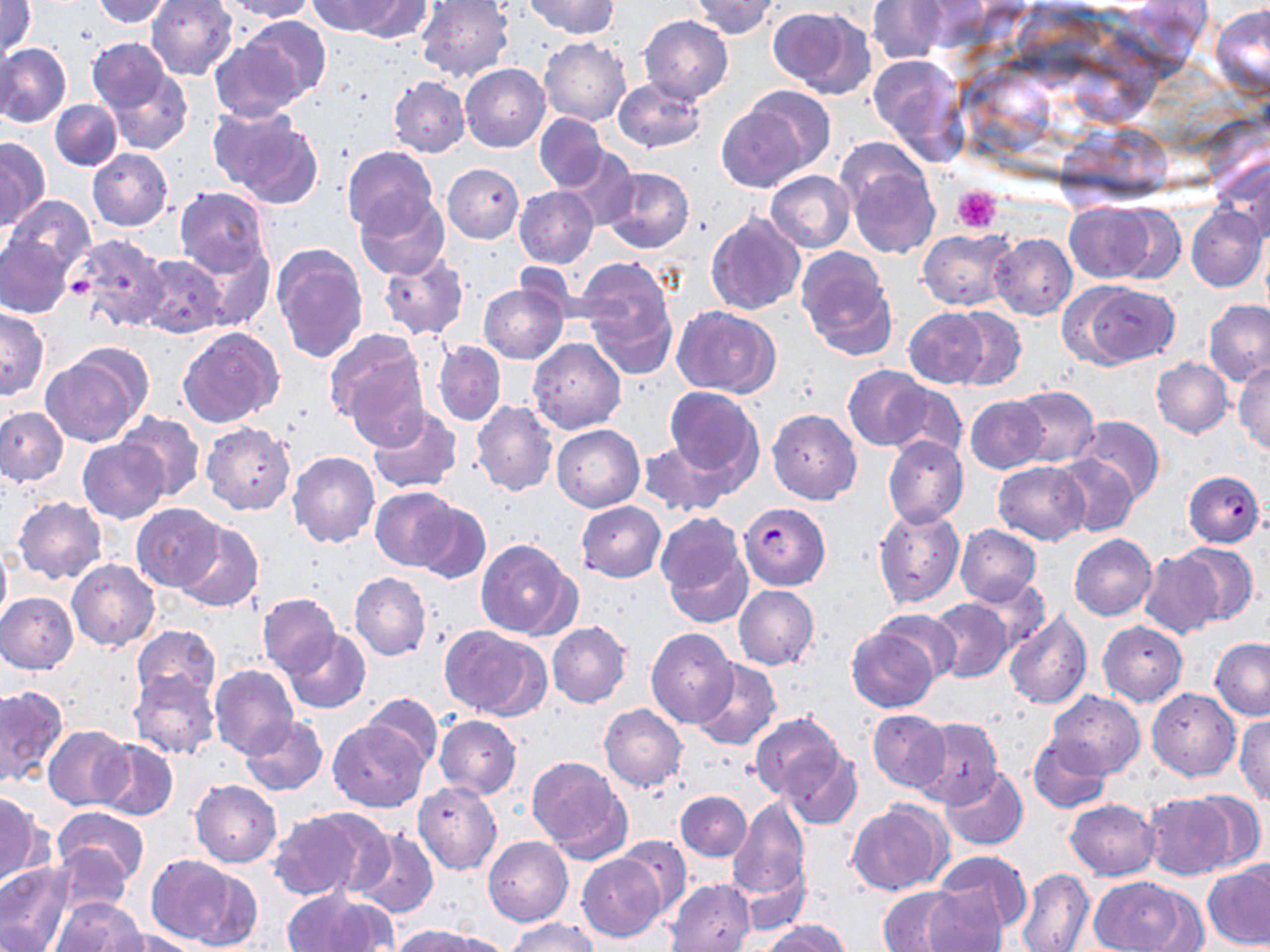

Summary:
  - Coordinate format: approximate bounding boxes as [x1, y1, x2, y2] in pixels
  - Plasmodium falciparum-infected red blood cell locations: [1183, 470, 1265, 546], [738, 501, 831, 590]
  - Platelet locations: [951, 186, 1003, 236], [68, 277, 97, 300]
  - Uninfected red blood cell locations: [92, 0, 172, 26], [146, 0, 239, 81], [219, 0, 315, 21], [306, 0, 406, 36], [343, 0, 432, 40], [523, 0, 619, 39], [689, 0, 780, 39], [867, 0, 946, 64], [1, 1, 37, 62], [415, 1, 514, 81], [1212, 4, 1269, 97], [768, 5, 876, 99], [238, 15, 333, 108], [639, 15, 733, 104], [539, 37, 631, 126], [87, 38, 169, 111], [209, 39, 306, 122], [0, 40, 18, 121], [1, 43, 72, 128], [867, 53, 970, 162], [461, 63, 551, 153], [107, 67, 192, 155], [98, 68, 182, 230], [388, 77, 469, 158], [614, 78, 706, 152], [715, 98, 812, 192], [50, 100, 122, 170], [209, 106, 322, 207], [535, 114, 608, 191], [0, 136, 49, 228], [560, 144, 638, 231], [341, 146, 437, 235], [87, 148, 173, 231], [1213, 153, 1270, 243], [843, 156, 939, 258], [443, 163, 524, 243], [602, 166, 693, 254], [766, 170, 855, 253], [174, 186, 271, 278], [515, 186, 599, 268], [355, 190, 450, 279], [4, 197, 93, 278], [1065, 204, 1156, 283], [1105, 205, 1185, 284], [1186, 206, 1268, 292], [706, 212, 804, 315], [918, 229, 1016, 310], [69, 233, 169, 331], [990, 234, 1077, 321], [1, 237, 74, 317], [272, 244, 369, 363], [188, 245, 274, 330], [795, 249, 896, 359], [376, 250, 468, 341], [136, 254, 226, 338], [574, 257, 678, 372], [1069, 281, 1177, 369], [478, 283, 570, 363], [1203, 300, 1270, 386], [672, 306, 780, 396], [903, 307, 989, 388], [949, 307, 1026, 391], [0, 309, 49, 400], [178, 326, 284, 427], [325, 329, 428, 436], [529, 339, 625, 434], [433, 341, 506, 427], [41, 347, 151, 446], [1152, 357, 1233, 437], [1234, 361, 1269, 455], [843, 366, 930, 451], [883, 383, 967, 464], [1010, 385, 1099, 467], [665, 386, 760, 483], [965, 396, 1048, 473], [472, 402, 558, 497], [367, 406, 462, 494], [0, 407, 68, 487], [768, 409, 862, 505], [116, 412, 205, 501], [1073, 415, 1163, 504], [202, 422, 295, 515], [552, 424, 644, 511], [882, 436, 969, 528], [77, 437, 169, 524], [638, 438, 734, 516], [288, 452, 380, 548], [1052, 452, 1137, 537], [994, 461, 1091, 545], [370, 487, 460, 572], [13, 497, 107, 584], [413, 499, 490, 584], [576, 501, 666, 581], [132, 503, 225, 591], [873, 506, 964, 609], [656, 511, 751, 624], [173, 520, 264, 613], [955, 524, 1041, 605], [1069, 533, 1157, 620], [475, 539, 579, 640], [0, 542, 11, 631], [1171, 542, 1258, 626], [1139, 551, 1222, 638], [66, 558, 160, 650], [350, 572, 431, 660], [965, 577, 1046, 655], [733, 585, 819, 670], [0, 592, 78, 674], [257, 593, 341, 676], [928, 598, 1011, 682], [872, 606, 963, 683], [1004, 610, 1092, 710], [1098, 620, 1188, 706], [547, 621, 631, 707], [130, 625, 220, 706], [846, 625, 940, 713], [443, 626, 551, 720], [646, 628, 737, 728], [283, 629, 370, 714], [1209, 638, 1270, 719], [691, 659, 780, 750], [209, 664, 298, 757], [129, 672, 219, 759], [0, 686, 66, 787], [1147, 688, 1240, 780], [1047, 690, 1143, 778], [360, 693, 442, 772], [600, 704, 687, 792], [868, 709, 951, 793], [749, 712, 848, 807], [435, 715, 521, 799], [1234, 715, 1270, 805], [240, 717, 328, 797], [911, 718, 1002, 807], [329, 720, 425, 812], [42, 725, 132, 810], [1027, 732, 1113, 814], [94, 740, 177, 821], [780, 747, 862, 829], [527, 755, 631, 860], [940, 766, 1028, 851], [189, 780, 282, 867], [413, 781, 502, 875], [676, 789, 752, 860], [1188, 789, 1267, 870], [0, 793, 45, 883], [1142, 793, 1238, 879], [728, 797, 812, 905], [1066, 799, 1159, 879], [847, 801, 950, 896], [52, 805, 149, 886], [268, 809, 382, 899], [352, 829, 439, 919], [613, 835, 691, 919], [483, 837, 573, 926], [47, 841, 134, 917], [931, 850, 1033, 938], [578, 854, 668, 942], [145, 855, 245, 948], [0, 862, 73, 951], [1202, 862, 1270, 950], [1017, 869, 1094, 952], [1091, 876, 1200, 951], [664, 879, 755, 951], [875, 885, 981, 952], [284, 889, 393, 952], [49, 898, 146, 951], [503, 917, 598, 952], [759, 921, 850, 952], [394, 925, 502, 952], [108, 927, 203, 952]
  - Slide-level diagnosis: Plasmodium falciparum
  - Image size: 1270×952 pixels
  - Modality: light microscopy
  - Stain: May-Grünwald-Giemsa
  - Field of view: one of a larger specimen
  - Preparation: thin blood smear
  - Magnification: 1000x